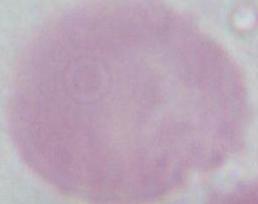

Summary:
  - Modality: micrograph
  - Magnification: 1000x
  - Identification: erythrocyte